Assess for malaria.
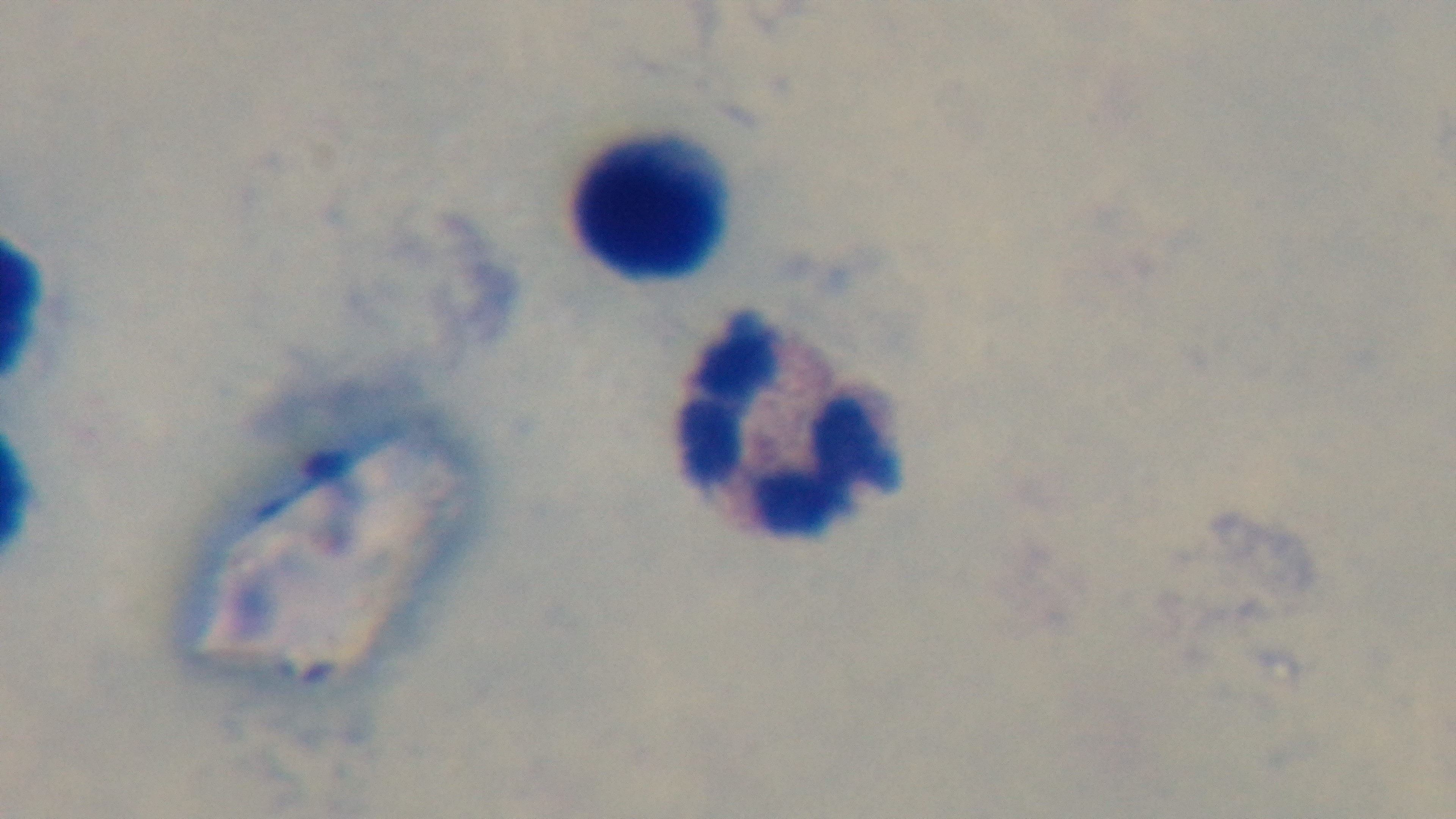
It is uninfected.

Captured with a mounted 4K digital camera. Preparation: thick smear. Giemsa-stained. Photomicrograph. 100x oil-immersion objective. One field from the slide.